Look for Plasmodium parasites.
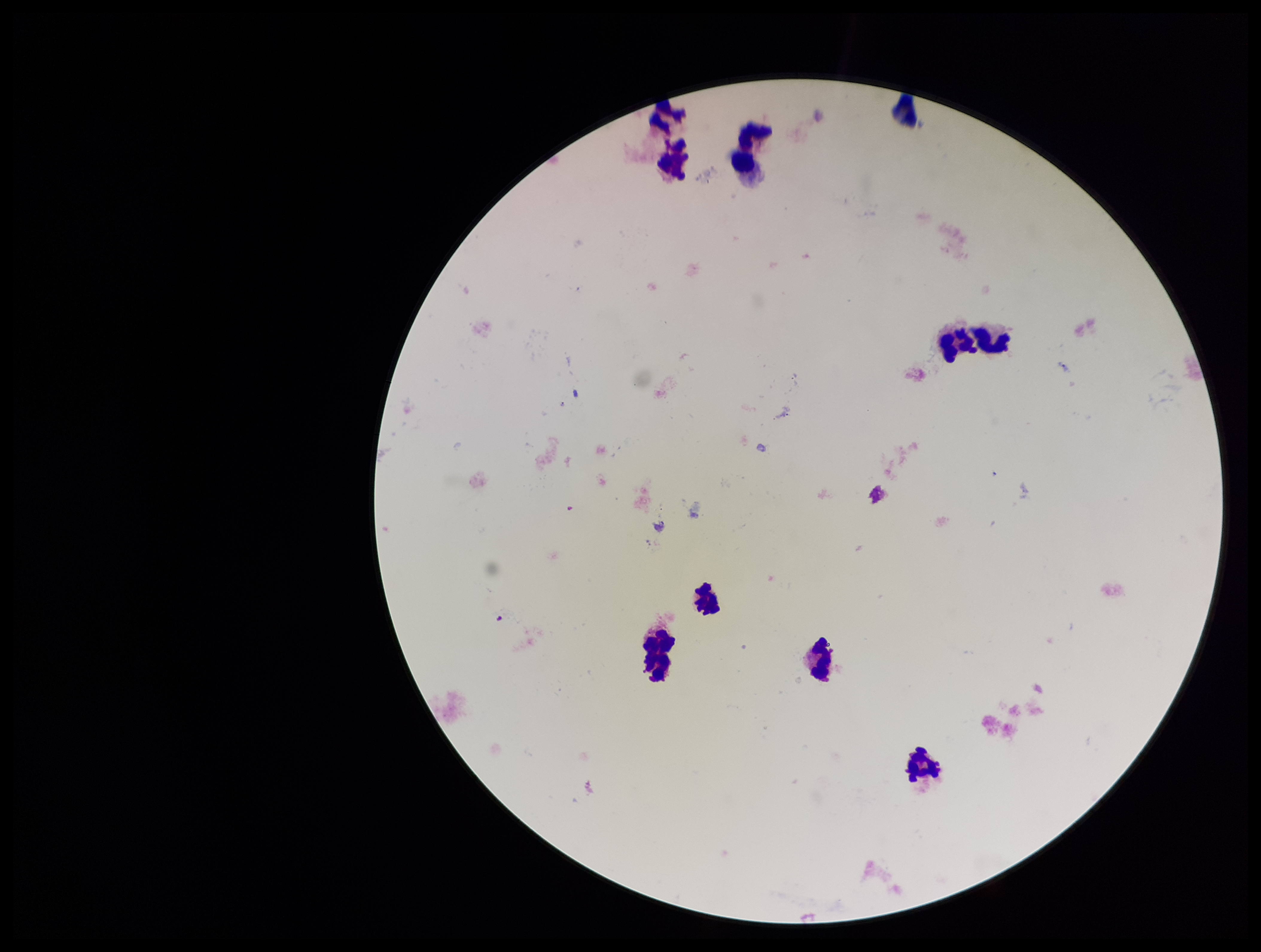
None detected.

Preparation: thick blood smear. Parasite count: 0. Single field of view. Patient malaria status: negative. Leukocyte count: 10. Smartphone photograph taken through the eyepiece of a microscope. Image is 1261×952 pixels. Giemsa stain.